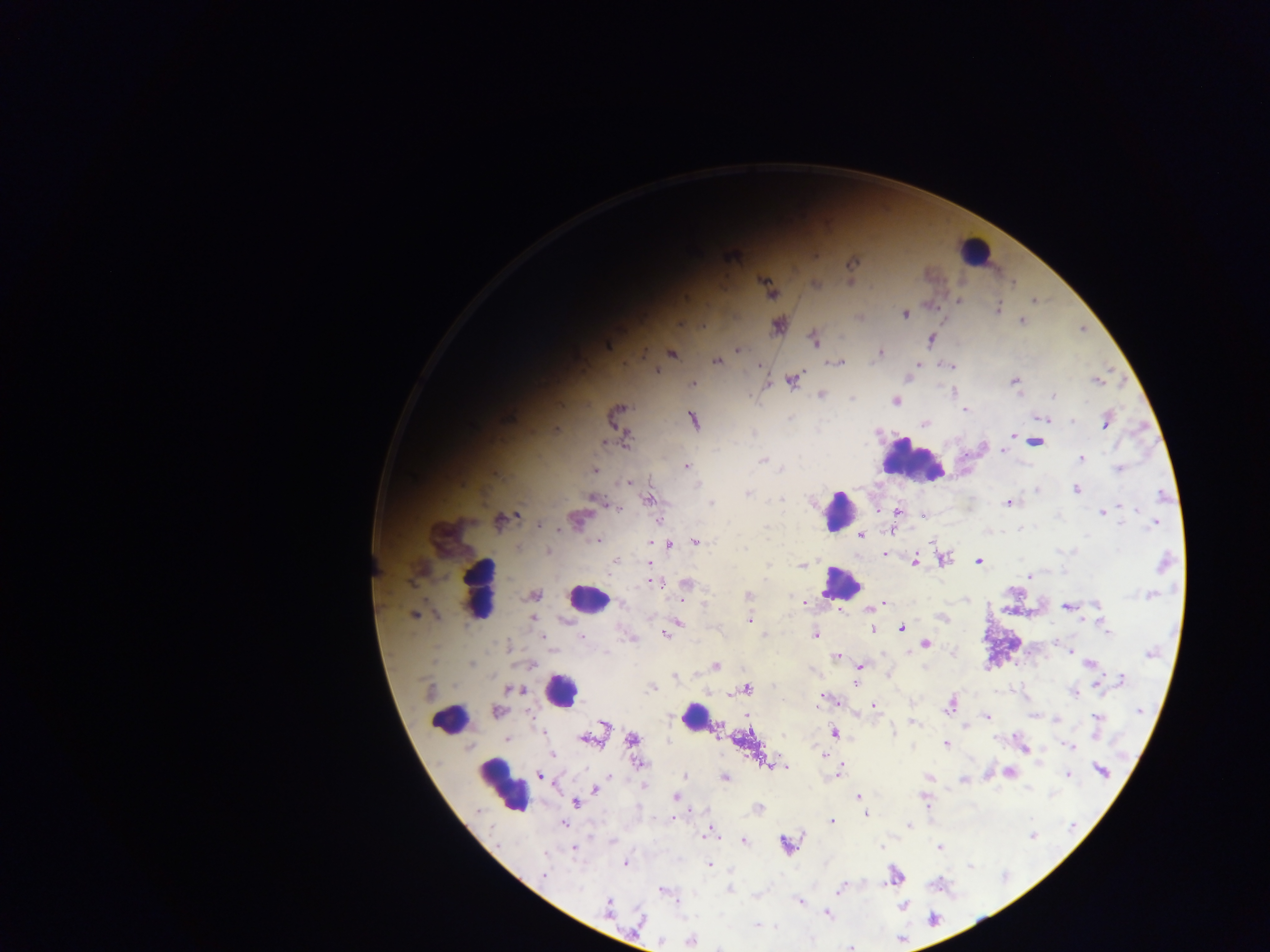

capture = mobile-phone photograph through a microscope
country = Ghana
Plasmodium parasite locations = approximate centers as {x, y} in pixels: {851, 262}, {816, 285}, {958, 301}, {1033, 301}, {998, 309}, {904, 314}, {1022, 321}, {679, 323}, {778, 326}, {814, 339}, {931, 339}, {608, 344}, {738, 350}, {880, 352}, {671, 353}, {717, 361}, {836, 363}, {917, 365}, {950, 366}, {655, 370}, {910, 377}, {792, 379}, {1014, 381}, {1097, 381}, {693, 384}, {954, 391}, {821, 396}, {1053, 396}, {852, 399}, {895, 400}, {966, 410}, {614, 416}, {1039, 418}, {1046, 420}, {693, 421}, {1072, 421}, {1107, 421}, {925, 423}, {1012, 435}, {626, 441}, {1035, 442}, {1003, 450}, {1081, 459}, {763, 460}, {686, 467}, {782, 469}, {1119, 469}, {595, 470}, {626, 482}, {1037, 490}, {1076, 490}, {748, 493}, {1163, 495}, {782, 499}, {594, 500}, {648, 500}, {1009, 502}, {711, 503}, {1120, 506}, {617, 508}, {1135, 509}, {898, 511}, {1102, 511}, {500, 521}, {576, 521}, {1153, 523}, {540, 525}, {1022, 528}, {892, 530}, {861, 535}, {598, 540}, {695, 542}, {670, 545}, {744, 549}, {548, 551}, {885, 554}, {943, 559}, {914, 561}, {979, 561}, {616, 562}, {649, 563}, {1164, 564}, {803, 565}, {1029, 576}, {655, 582}, {687, 583}, {749, 594}, {535, 595}, {1151, 595}, {804, 603}, {882, 604}, {1068, 607}, {1097, 607}, {872, 608}, {414, 616}, {942, 618}, {533, 620}, {749, 620}, {564, 621}, {678, 623}, {902, 627}, {872, 628}, {1107, 631}, {665, 634}, {815, 635}, {542, 636}, {581, 636}, {926, 643}, {1069, 652}, {1150, 654}, {836, 656}, {1090, 664}, {471, 665}, {715, 666}, {860, 666}, {675, 676}, {1122, 680}, {855, 683}, {1098, 683}, {651, 687}, {746, 689}, {516, 690}, {429, 692}, {1074, 693}, {828, 700}, {950, 705}, {874, 706}, {1139, 710}, {497, 712}, {987, 717}, {1097, 718}, {914, 723}, {603, 725}, {893, 731}, {835, 733}, {507, 739}, {633, 739}, {587, 740}, {946, 744}, {1069, 746}, {553, 754}, {823, 754}, {769, 763}, {640, 764}, {780, 766}, {1101, 770}, {839, 772}, {1009, 773}, {540, 775}, {1068, 775}, {684, 776}, {928, 777}, {726, 778}, {963, 779}, {643, 785}, {595, 790}, {859, 795}, {675, 796}, {924, 799}, {576, 802}, {759, 808}, {866, 814}, {831, 822}, {564, 824}, {909, 824}, {710, 833}, {1032, 835}, {744, 841}, {786, 845}, {882, 847}, {938, 847}, {573, 849}, {625, 863}, {710, 865}, {544, 874}, {895, 876}, {729, 889}, {840, 889}, {663, 890}, {799, 903}, {608, 906}, {903, 906}, {827, 914}, {932, 919}, {640, 921}, {758, 926}, {691, 940}, {851, 948}
preparation = thick blood film
image size = 1270×952 pixels
leukocyte locations = approximate centers as {x, y} in pixels: {975, 249}, {913, 462}, {839, 511}, {841, 583}, {481, 591}, {587, 599}, {561, 691}, {450, 715}, {697, 717}, {503, 787}
field of view = single